Give the position of every Plasmodium parasite visible.
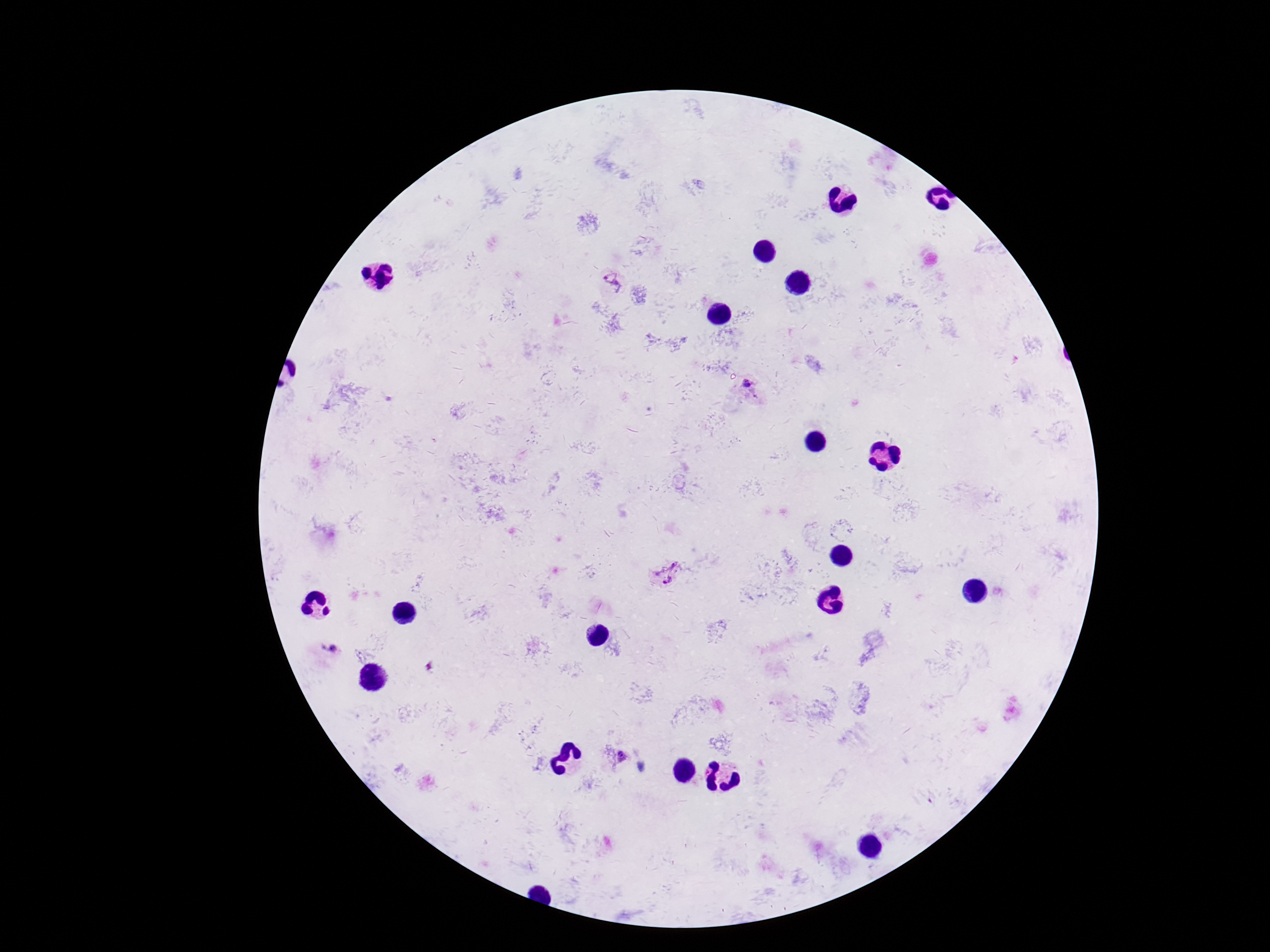

Approximate centers as {x, y} in pixels.
Plasmodium parasites: {613, 283}, {745, 384}, {666, 574}, {329, 649}, {621, 758}.

Giemsa stain. Photographed through the microscope eyepiece with a smartphone camera. Patient malaria status: positive. Image is 1270×952 pixels. 100x magnification. One field from this slide. Thick blood smear.